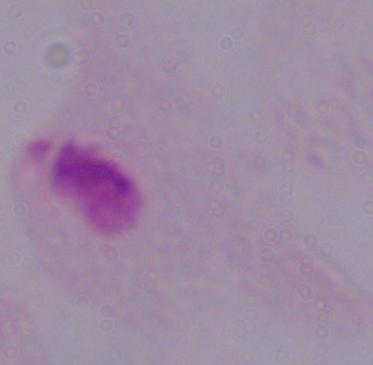

Photomicrograph. A trichomonad is shown. Captured at 1000x magnification.